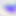

Micrograph. Toxoplasma gondii is shown. Captured at 400x magnification.